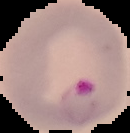

Summary:
  - Preparation: thin blood smear
  - Image size: 130×133 pixels
  - Result: Plasmodium parasites identified
  - Image type: cell region segmented out of the field of view; surrounding area masked to black